Classify this cell by malaria status.
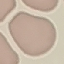
It is uninfected.

preparation = thin blood smear
image type = cell patch, automatically extracted from a larger field of view and resized to 64 × 64 pixels
stain = Giemsa
capture = smartphone camera at the microscope eyepiece